Locate and identify every blood parasite.
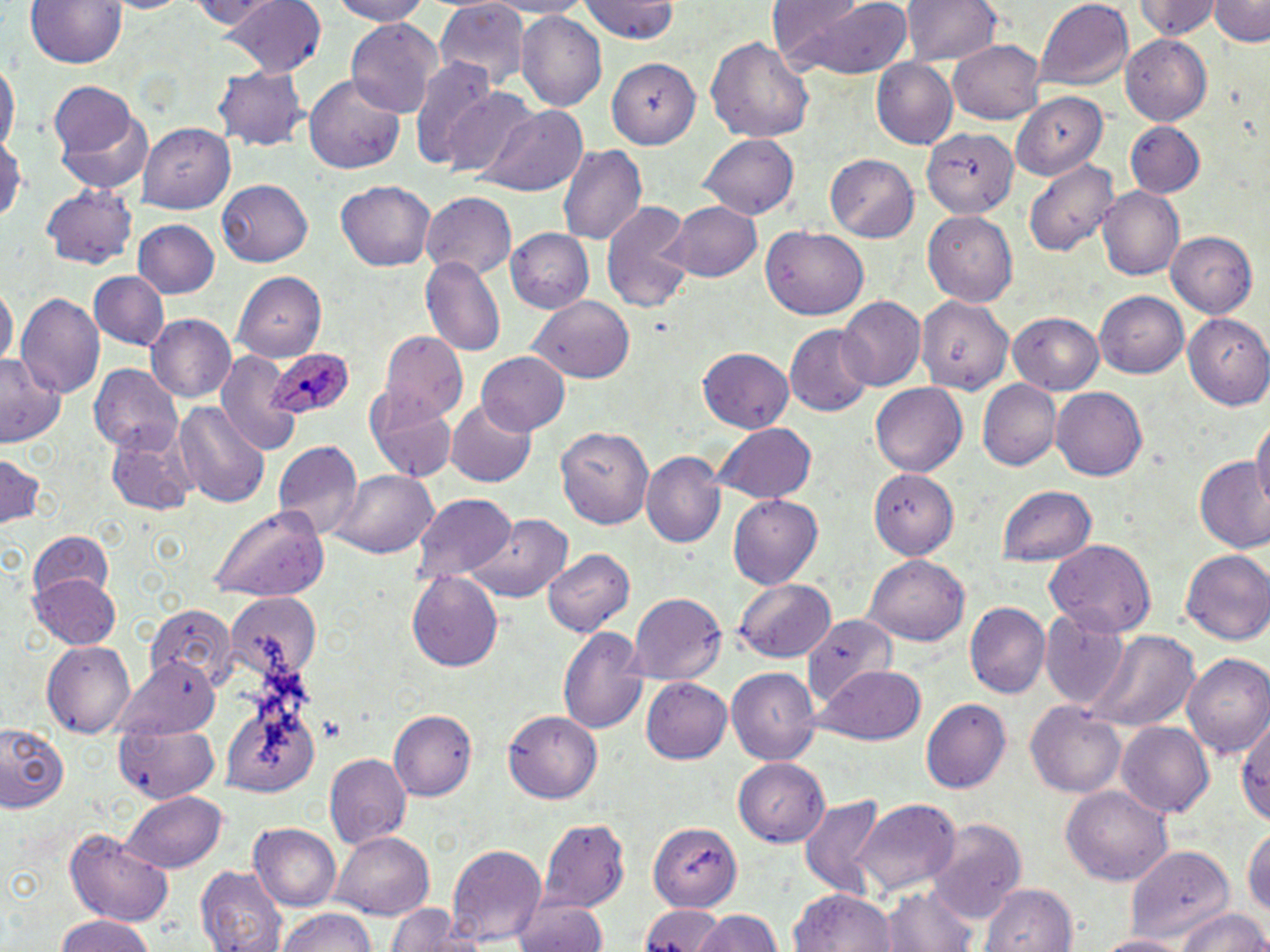
Approximate bounding boxes as [x1, y1, x2, y2] in pixels.
Plasmodium ovale-infected red blood cells: [263, 349, 355, 423].
No Plasmodium falciparum, Plasmodium malariae, Plasmodium vivax, Babesia divergens, or Trypanosoma brucei observed.

Summary:
  - Uninfected red blood cell locations: [29, 0, 126, 69], [103, 0, 199, 17], [179, 0, 281, 29], [224, 0, 327, 77], [323, 0, 433, 25], [434, 0, 532, 92], [492, 0, 597, 17], [580, 0, 682, 43], [774, 0, 914, 79], [899, 0, 1003, 68], [1133, 0, 1220, 40], [1210, 0, 1270, 47], [1036, 1, 1135, 91], [517, 11, 607, 112], [345, 19, 440, 115], [1120, 30, 1213, 124], [706, 33, 815, 145], [950, 39, 1046, 124], [603, 52, 704, 148], [0, 56, 17, 162], [410, 59, 498, 170], [869, 59, 958, 150], [214, 65, 308, 151], [303, 74, 408, 177], [48, 82, 136, 157], [442, 87, 538, 177], [1012, 92, 1109, 177], [478, 105, 588, 196], [57, 111, 155, 194], [1125, 122, 1205, 197], [140, 124, 236, 213], [915, 125, 1023, 222], [0, 133, 24, 225], [700, 136, 798, 220], [557, 143, 648, 243], [826, 153, 921, 240], [1023, 160, 1118, 257], [217, 179, 313, 267], [335, 179, 437, 272], [42, 185, 136, 270], [1097, 186, 1186, 280], [421, 193, 516, 280], [668, 199, 763, 283], [601, 202, 695, 312], [924, 212, 1017, 307], [134, 219, 219, 300], [761, 228, 868, 320], [504, 229, 592, 313], [1167, 231, 1258, 318], [420, 255, 505, 354], [91, 272, 168, 350], [233, 272, 327, 358], [0, 284, 16, 374], [1094, 291, 1189, 379], [916, 293, 1012, 394], [16, 294, 104, 402], [530, 296, 635, 382], [836, 297, 925, 390], [1008, 312, 1106, 395], [1184, 314, 1270, 409], [148, 315, 240, 402], [786, 326, 873, 416], [381, 329, 465, 419], [697, 347, 794, 432], [0, 351, 66, 448], [215, 353, 298, 453], [475, 353, 570, 435], [90, 365, 181, 455], [978, 380, 1061, 469], [870, 384, 967, 475], [1051, 386, 1148, 481], [367, 394, 457, 482], [173, 399, 270, 507], [449, 402, 538, 487], [1252, 413, 1270, 518], [555, 421, 656, 529], [710, 423, 818, 504], [106, 429, 198, 517], [274, 441, 361, 540], [0, 451, 47, 529], [645, 452, 727, 548], [1193, 455, 1270, 556], [333, 468, 439, 559], [871, 470, 959, 561], [994, 485, 1098, 567], [410, 493, 517, 584], [728, 496, 823, 589], [207, 507, 331, 603], [469, 514, 572, 603], [27, 528, 115, 609], [1045, 540, 1157, 638], [542, 548, 633, 636], [1182, 549, 1270, 648], [865, 555, 969, 647], [406, 572, 503, 672], [30, 574, 120, 649], [735, 579, 835, 662], [227, 593, 322, 684], [628, 593, 725, 683], [964, 603, 1050, 698], [145, 604, 237, 688], [1041, 608, 1130, 709], [804, 613, 895, 712], [557, 624, 648, 735], [1085, 630, 1202, 735], [42, 640, 135, 737], [1182, 654, 1270, 762], [112, 660, 223, 744], [817, 664, 926, 745], [725, 667, 819, 764], [643, 676, 732, 764], [920, 699, 1008, 790], [1026, 700, 1129, 797], [388, 708, 477, 798], [503, 709, 603, 803], [1236, 716, 1270, 827], [115, 719, 218, 804], [1119, 722, 1215, 822], [0, 724, 69, 809], [326, 754, 410, 849], [736, 758, 830, 847], [1063, 786, 1170, 888], [120, 793, 227, 872], [796, 795, 889, 899], [852, 799, 960, 894], [647, 817, 746, 909], [538, 818, 629, 911], [927, 819, 1026, 923], [249, 825, 341, 912], [1242, 828, 1270, 922], [64, 829, 176, 924], [332, 832, 435, 918], [446, 843, 547, 943], [1126, 844, 1235, 941], [195, 865, 290, 952], [882, 881, 981, 952], [979, 881, 1078, 952], [791, 888, 896, 952], [511, 898, 609, 952], [384, 902, 465, 951], [638, 903, 728, 952], [1174, 907, 1270, 952], [275, 908, 379, 952], [690, 909, 787, 952], [50, 914, 160, 952], [1095, 931, 1190, 952]
  - Slide-level diagnosis: Plasmodium ovale
  - Image size: 1270×952 pixels
  - Preparation: thin blood film
  - Field of view: single
  - Modality: light microscopy
  - Stain: May-Grünwald-Giemsa
  - Magnification: 1000x